Classify this cell by malaria status.
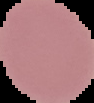
Uninfected.

Summary:
  - Image size: 94×103 pixels
  - Preparation: thin blood film
  - Image type: segmented cell region on a black background